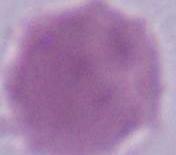
Photomicrograph. Captured at 1000x magnification. An erythrocyte is seen.